Classify this cell by malaria status.
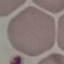
It is uninfected.

Summary:
  - Capture: smartphone through the microscope eyepiece
  - Image type: cell patch, automatically extracted from a larger field of view and resized to 64 × 64 pixels
  - Preparation: thin smear
  - Stain: Giemsa